Locate and identify every blood parasite.
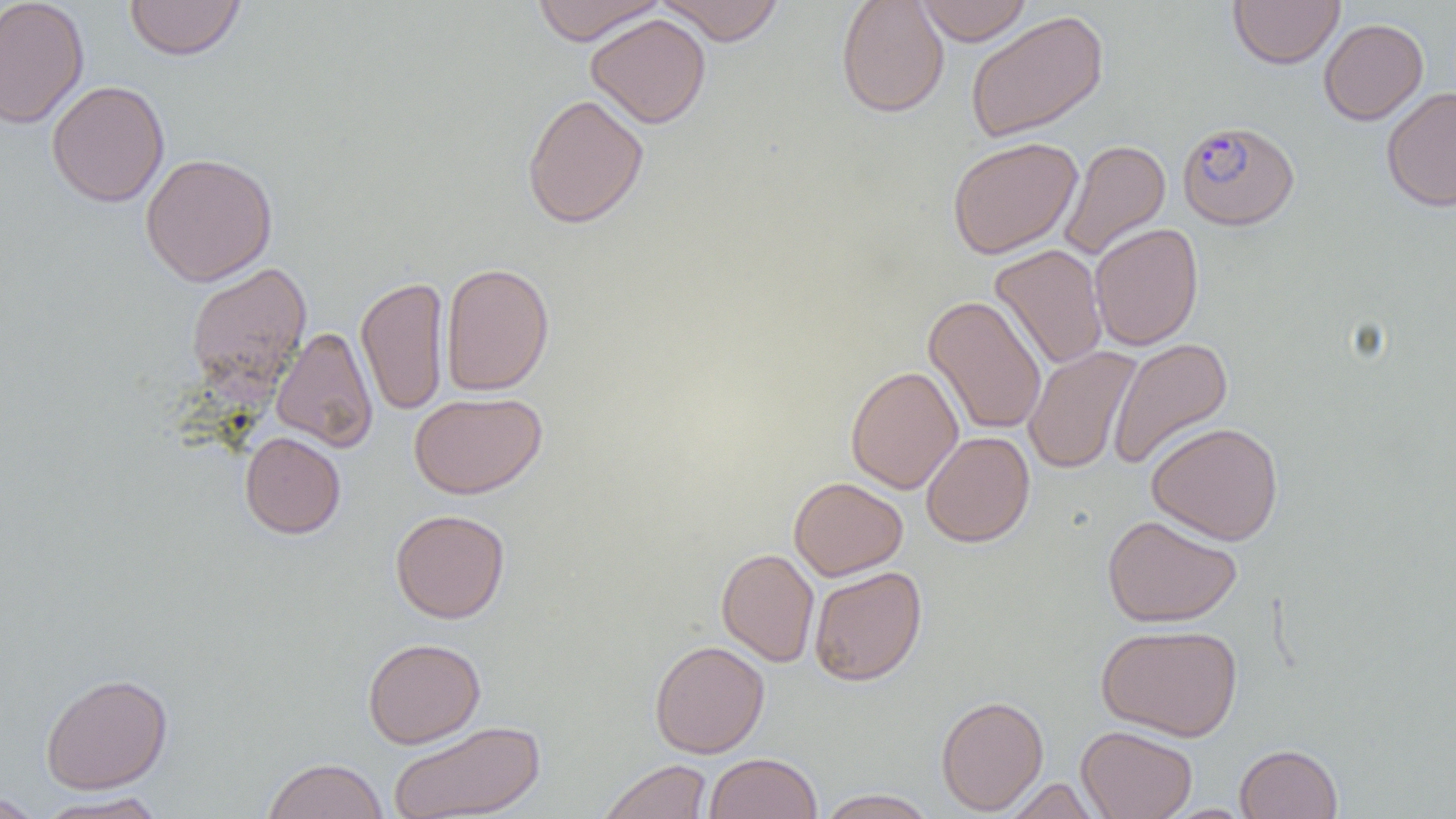

Approximate bounding boxes as (x1, y1, x2, y2) in pixels.
Plasmodium falciparum-infected red blood cells: (1177, 120, 1299, 230).
No Plasmodium ovale, Plasmodium malariae, Plasmodium vivax, Babesia divergens, or Trypanosoma brucei observed.

Uninfected red blood cell locations: (0, 0, 90, 129), (530, 0, 666, 45), (655, 0, 786, 45), (836, 0, 949, 118), (915, 0, 1033, 45), (1228, 0, 1344, 70), (124, 1, 246, 61), (965, 9, 1109, 144), (585, 13, 711, 129), (1318, 18, 1428, 125), (46, 80, 170, 207), (1381, 87, 1456, 212), (522, 93, 649, 229), (947, 136, 1082, 259), (1059, 139, 1171, 261), (140, 152, 278, 286), (1089, 223, 1204, 351), (990, 244, 1107, 370), (185, 262, 312, 399), (440, 262, 555, 396), (356, 276, 450, 416), (923, 295, 1047, 435), (270, 326, 378, 452), (1107, 337, 1234, 470), (1023, 345, 1142, 475), (845, 365, 964, 494), (409, 391, 547, 499), (1146, 421, 1284, 545), (921, 431, 1035, 547), (239, 432, 346, 539), (789, 476, 908, 580), (390, 509, 510, 623), (1102, 514, 1242, 627), (716, 548, 819, 667), (809, 565, 928, 686), (1096, 623, 1242, 741), (362, 637, 486, 748), (649, 640, 770, 758), (40, 672, 173, 794), (936, 695, 1048, 815), (387, 720, 546, 819), (1076, 725, 1197, 819), (1235, 743, 1343, 818), (704, 752, 822, 819), (262, 757, 389, 819), (598, 759, 712, 819), (1004, 778, 1101, 818), (816, 788, 938, 818), (0, 791, 45, 818), (34, 791, 169, 818). Slide-level diagnosis: Plasmodium falciparum. Optical microscopy. Thin blood smear. Single field of view. Captured at 1000x magnification. Image is 1456×819 pixels.